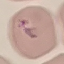
Malaria status: uninfected. Thin smear of blood. Cell patch, automatically extracted from a larger field of view and resized to 64 × 64 pixels. Acquired by smartphone through the microscope eyepiece. Giemsa stain.